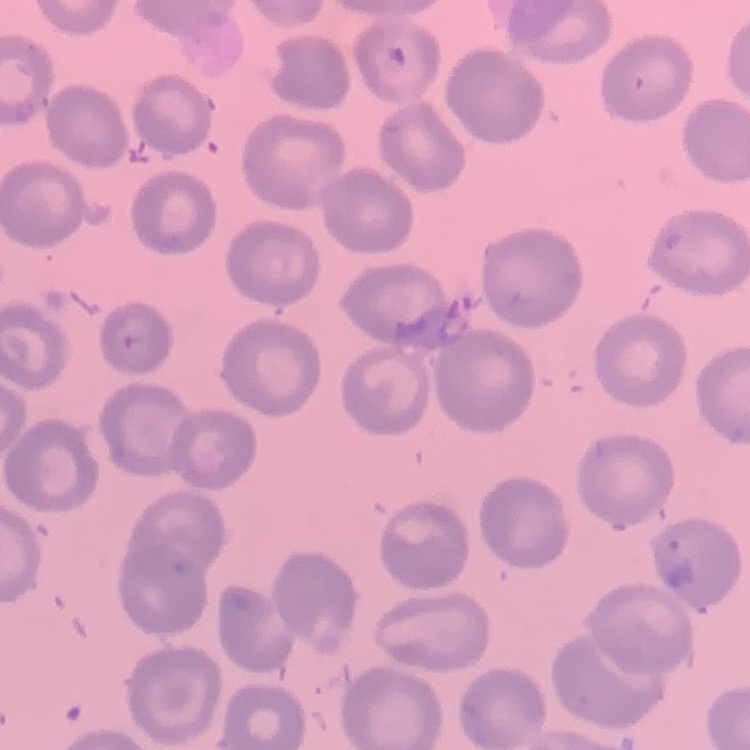
The erythrocytes exhibit no rouleaux formation. Stained with either Field's or Giemsa. Square crop of a larger photomicrograph. Thin peripheral smear.